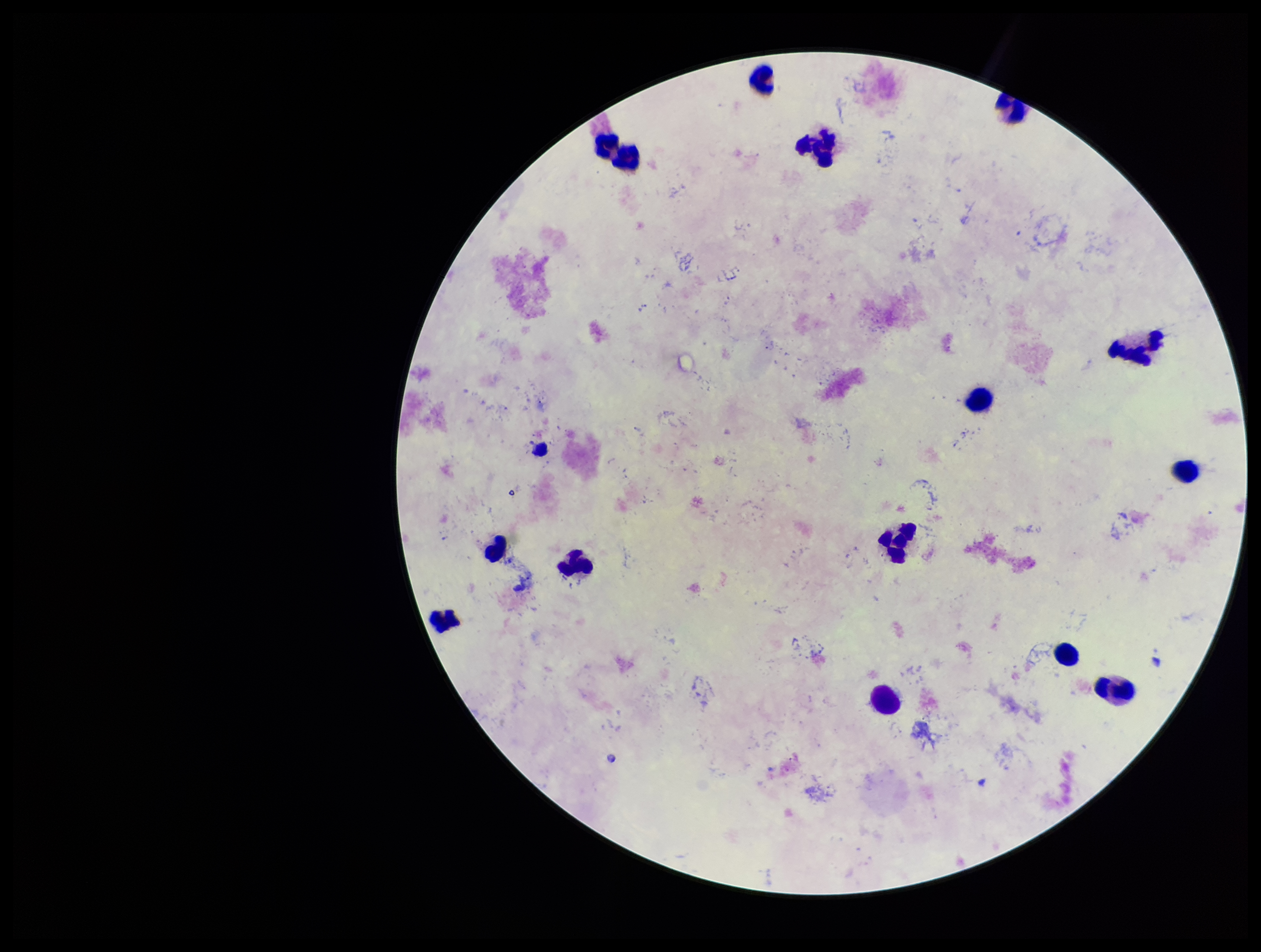
Summary:
  - Species reported for this patient: Plasmodium vivax
  - Stain: Giemsa
  - Preparation: thick
  - Plasmodium parasites: none identified
  - Parasite count: 0
  - Image size: 1261×952 pixels
  - Patient malaria status: infected
  - Leukocyte count: 16
  - Capture: smartphone photograph through the microscope eyepiece
  - Field of view: one from this slide